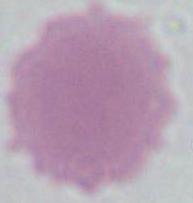

modality = photomicrograph
identification = erythrocyte
magnification = 1000x